Assess this cell for malaria.
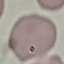
Uninfected.

Thin blood film. Cell patch, automatically extracted from a larger field of view and resized to 64 × 64 pixels. Giemsa stain. Acquired by smartphone through the microscope eyepiece.